Point out each Plasmodium parasite.
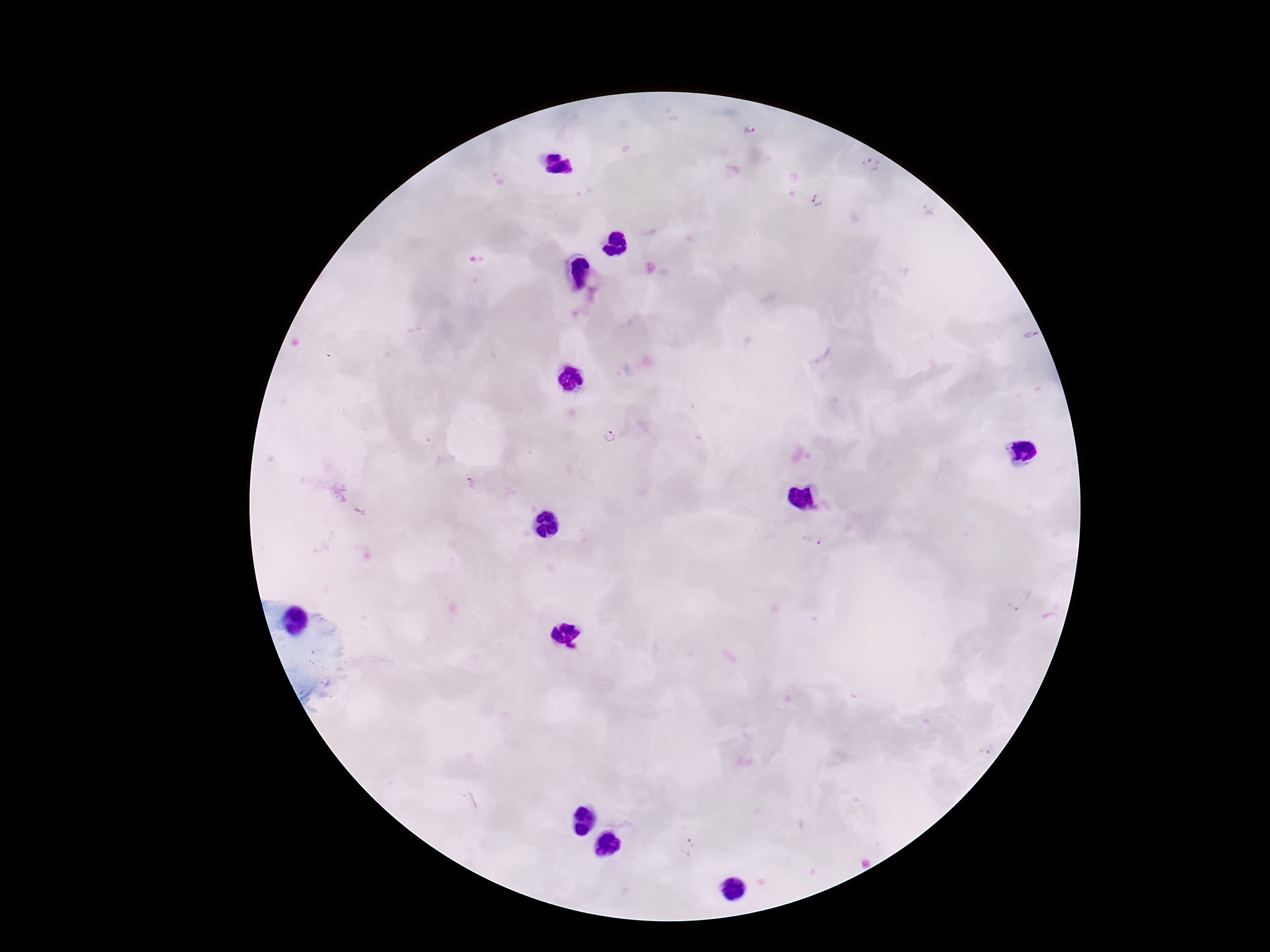

Approximate centers as [x, y] in pixels.
Plasmodium parasites: [750, 132], [870, 165], [818, 200], [930, 211], [1030, 334], [609, 437], [471, 483], [358, 512], [812, 541], [1013, 605], [984, 754], [688, 847].

Image is 1270×952 pixels. Thick blood smear. 100x magnification. Smartphone photograph taken through the microscope eyepiece. One field from this slide. Giemsa stain. Patient malaria status: positive.